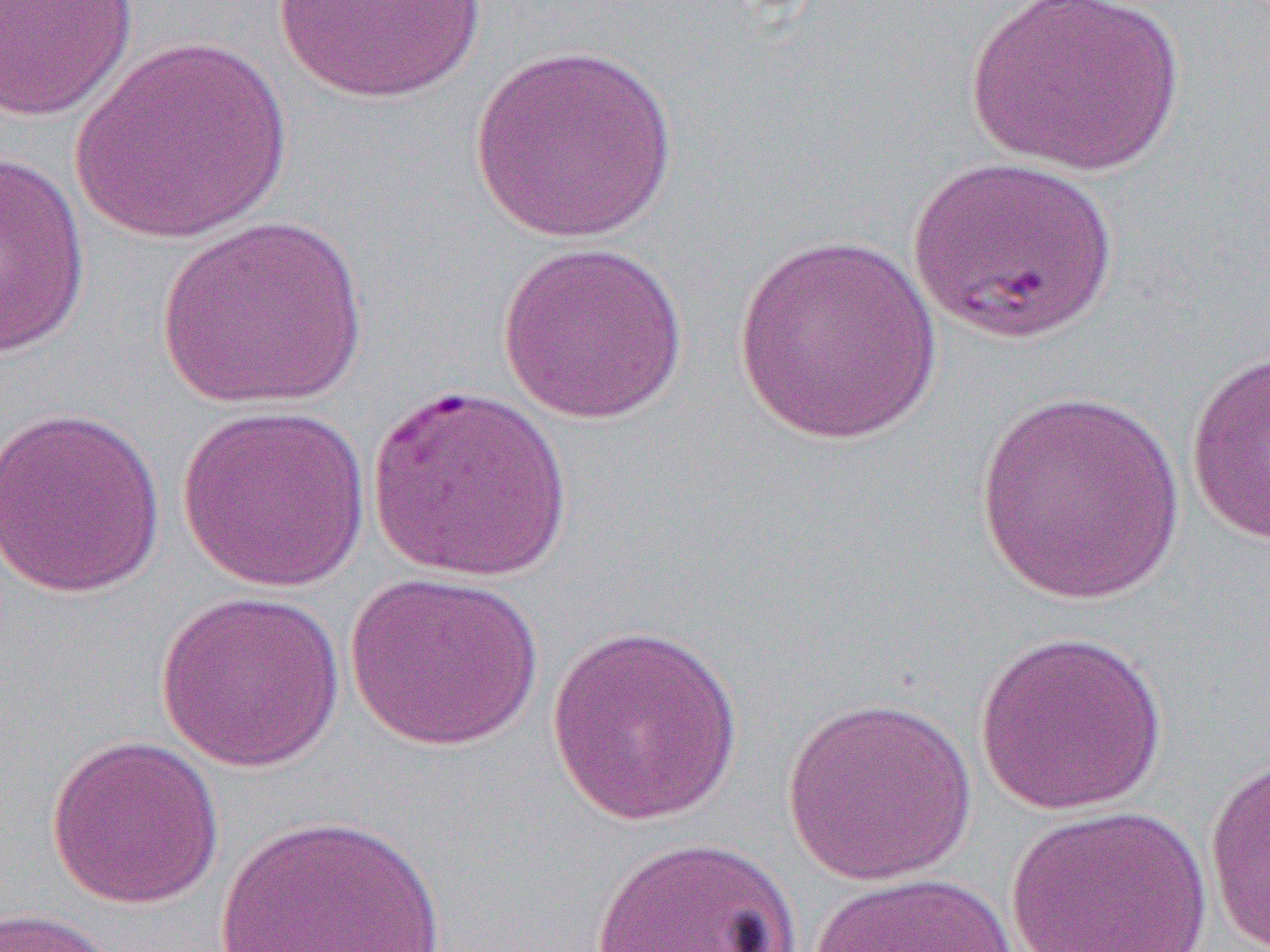
slide-level diagnosis = Plasmodium falciparum
magnification = 1000x
preparation = thin blood smear
modality = optical microscopy
field of view = one of a larger specimen
image size = 1270×952 pixels
uninfected red blood cell locations = approximate bounding boxes as named x1/y1/x2/y2 corners in pixels: (x1=268, y1=0, x2=494, y2=106), (x1=965, y1=0, x2=1186, y2=177), (x1=0, y1=1, x2=138, y2=123), (x1=71, y1=36, x2=294, y2=245), (x1=469, y1=43, x2=682, y2=244), (x1=0, y1=149, x2=92, y2=359), (x1=910, y1=154, x2=1119, y2=344), (x1=153, y1=213, x2=371, y2=411), (x1=732, y1=233, x2=944, y2=447), (x1=496, y1=239, x2=690, y2=425), (x1=1185, y1=352, x2=1270, y2=547), (x1=367, y1=382, x2=572, y2=583), (x1=973, y1=387, x2=1190, y2=606), (x1=0, y1=404, x2=167, y2=598), (x1=177, y1=404, x2=372, y2=592), (x1=343, y1=570, x2=544, y2=752), (x1=154, y1=589, x2=346, y2=772), (x1=546, y1=622, x2=745, y2=826), (x1=973, y1=629, x2=1169, y2=816), (x1=780, y1=695, x2=979, y2=885), (x1=46, y1=734, x2=225, y2=910), (x1=1203, y1=755, x2=1270, y2=952), (x1=1004, y1=804, x2=1213, y2=952), (x1=216, y1=811, x2=447, y2=952), (x1=589, y1=834, x2=805, y2=952), (x1=807, y1=871, x2=1022, y2=952), (x1=0, y1=907, x2=133, y2=952)